Identify the parasite.
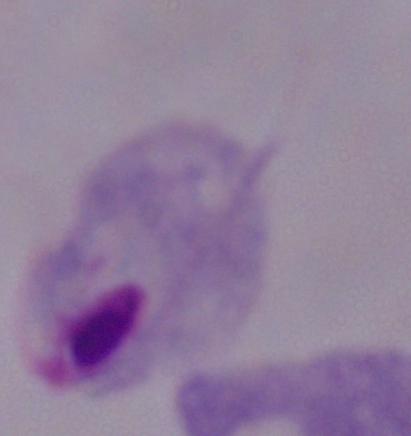

A trichomonad.

Summary:
  - Modality: micrograph
  - Magnification: 1000x